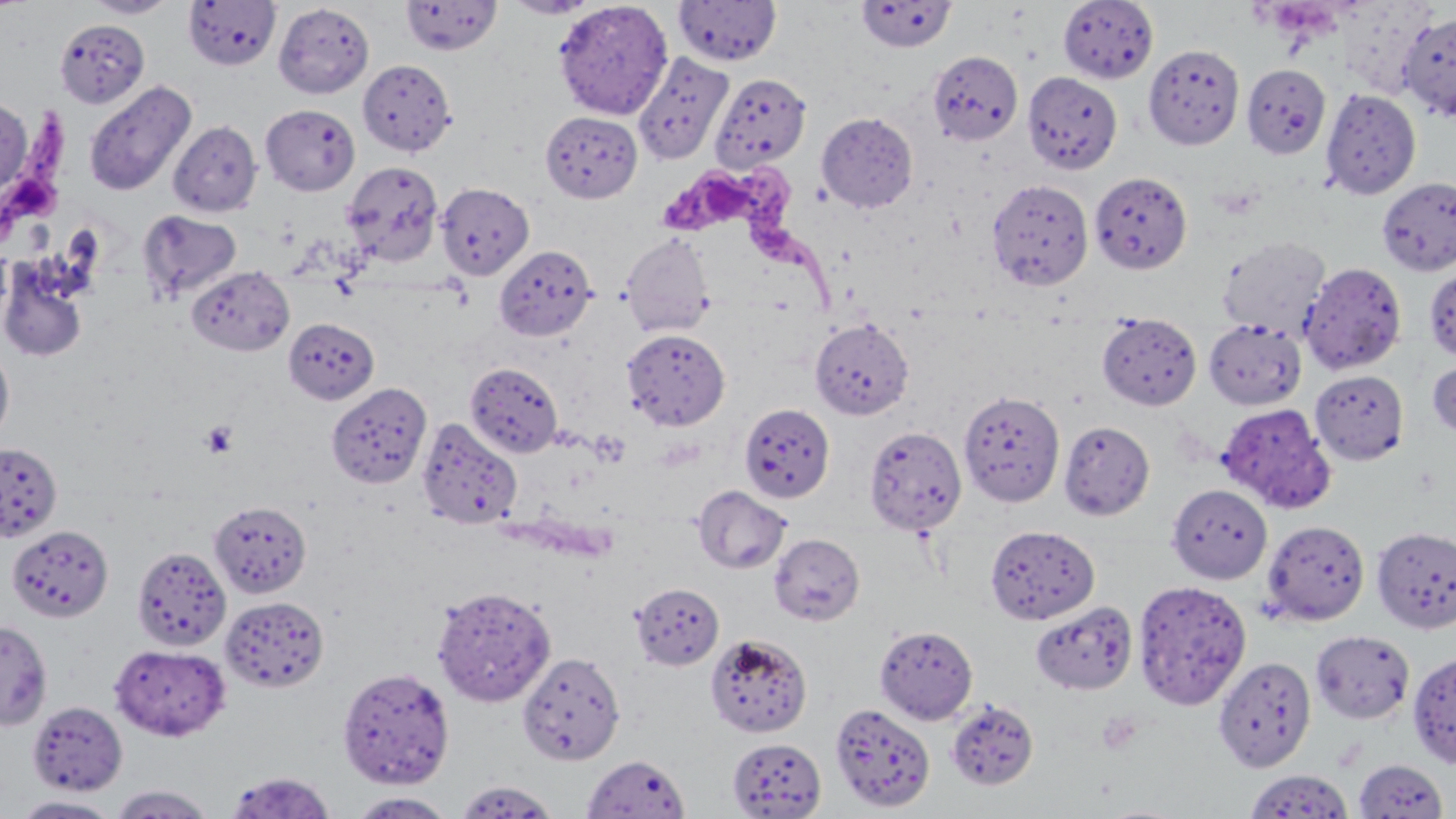

Approximate bounding boxes as named x1/y1/x2/y2 corners in pixels. Uninfected red blood cell locations: (x1=84, y1=0, x2=178, y2=18), (x1=183, y1=0, x2=280, y2=70), (x1=401, y1=0, x2=502, y2=55), (x1=503, y1=0, x2=599, y2=19), (x1=553, y1=0, x2=673, y2=119), (x1=674, y1=0, x2=782, y2=66), (x1=1058, y1=0, x2=1158, y2=83), (x1=856, y1=1, x2=957, y2=52), (x1=274, y1=3, x2=374, y2=98), (x1=1399, y1=12, x2=1456, y2=121), (x1=55, y1=19, x2=149, y2=108), (x1=1143, y1=44, x2=1244, y2=150), (x1=927, y1=50, x2=1023, y2=146), (x1=632, y1=52, x2=733, y2=165), (x1=357, y1=59, x2=456, y2=156), (x1=1242, y1=63, x2=1331, y2=158), (x1=1022, y1=71, x2=1123, y2=175), (x1=709, y1=72, x2=811, y2=173), (x1=84, y1=80, x2=196, y2=197), (x1=1320, y1=88, x2=1421, y2=200), (x1=0, y1=97, x2=31, y2=200), (x1=260, y1=104, x2=360, y2=196), (x1=541, y1=111, x2=642, y2=202), (x1=817, y1=112, x2=919, y2=213), (x1=169, y1=121, x2=262, y2=217), (x1=341, y1=160, x2=444, y2=267), (x1=1090, y1=171, x2=1192, y2=274), (x1=1377, y1=177, x2=1456, y2=276), (x1=986, y1=178, x2=1094, y2=291), (x1=437, y1=182, x2=534, y2=280), (x1=138, y1=209, x2=243, y2=303), (x1=620, y1=233, x2=717, y2=339), (x1=1218, y1=234, x2=1331, y2=339), (x1=494, y1=244, x2=596, y2=341), (x1=0, y1=261, x2=89, y2=362), (x1=1299, y1=262, x2=1407, y2=376), (x1=1424, y1=262, x2=1456, y2=363), (x1=188, y1=265, x2=294, y2=356), (x1=1097, y1=312, x2=1201, y2=410), (x1=810, y1=318, x2=913, y2=420), (x1=1203, y1=318, x2=1307, y2=410), (x1=283, y1=319, x2=379, y2=404), (x1=622, y1=328, x2=730, y2=431), (x1=0, y1=344, x2=15, y2=446), (x1=1427, y1=355, x2=1456, y2=443), (x1=465, y1=362, x2=563, y2=458), (x1=1310, y1=370, x2=1409, y2=464), (x1=327, y1=384, x2=432, y2=489), (x1=958, y1=389, x2=1065, y2=507), (x1=739, y1=403, x2=835, y2=502), (x1=1216, y1=403, x2=1336, y2=513), (x1=416, y1=417, x2=523, y2=530), (x1=1058, y1=420, x2=1155, y2=521), (x1=864, y1=426, x2=966, y2=535), (x1=0, y1=442, x2=63, y2=542), (x1=1167, y1=483, x2=1272, y2=584), (x1=693, y1=485, x2=791, y2=574), (x1=209, y1=501, x2=311, y2=598), (x1=1261, y1=519, x2=1369, y2=625), (x1=985, y1=524, x2=1099, y2=624), (x1=7, y1=525, x2=113, y2=622), (x1=1372, y1=525, x2=1456, y2=634), (x1=769, y1=533, x2=865, y2=625), (x1=131, y1=546, x2=231, y2=652), (x1=1133, y1=579, x2=1251, y2=711), (x1=630, y1=582, x2=724, y2=670), (x1=431, y1=586, x2=556, y2=706), (x1=220, y1=596, x2=329, y2=693), (x1=1030, y1=601, x2=1138, y2=694), (x1=0, y1=620, x2=53, y2=730), (x1=875, y1=625, x2=978, y2=724), (x1=1310, y1=630, x2=1415, y2=724), (x1=705, y1=633, x2=812, y2=737), (x1=109, y1=643, x2=231, y2=741), (x1=517, y1=651, x2=625, y2=765), (x1=1407, y1=651, x2=1456, y2=768), (x1=1213, y1=656, x2=1316, y2=772), (x1=337, y1=666, x2=455, y2=788), (x1=946, y1=698, x2=1039, y2=790), (x1=28, y1=701, x2=127, y2=796), (x1=830, y1=702, x2=935, y2=812), (x1=727, y1=737, x2=826, y2=818), (x1=582, y1=754, x2=691, y2=819), (x1=1353, y1=759, x2=1449, y2=818), (x1=1244, y1=769, x2=1353, y2=819), (x1=223, y1=771, x2=337, y2=818), (x1=454, y1=779, x2=560, y2=817), (x1=108, y1=784, x2=217, y2=818), (x1=347, y1=792, x2=457, y2=818), (x1=11, y1=795, x2=123, y2=817). Trypanosoma brucei locations: (x1=1, y1=108, x2=76, y2=247), (x1=660, y1=161, x2=847, y2=310). Platelet locations: (x1=1262, y1=3, x2=1342, y2=44), (x1=200, y1=421, x2=238, y2=458), (x1=1097, y1=711, x2=1142, y2=755). Slide-level diagnosis: Trypanosoma brucei. Captured at 1000x magnification. Single field of view. May-Grünwald-Giemsa stain. Image is 1456×819 pixels. Optical microscopy. Thin blood smear.